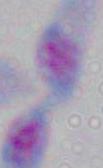

identification = Toxoplasma gondii
magnification = 1000x
modality = photomicrograph